Classify this cell by malaria status.
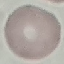

It is uninfected.

Giemsa stain. Photographed with a smartphone camera at the microscope eyepiece. Automatically extracted cell patch, resized to 64 × 64 pixels. Thin smear of blood.